Describe the morphology of the red blood cells.
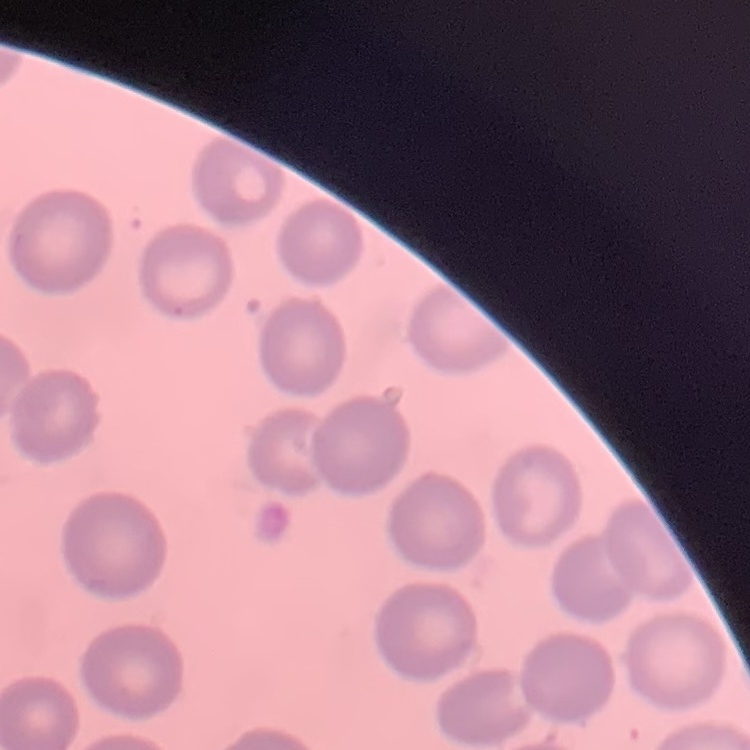
No rouleaux formation.

Thin blood film. One tile cut from a larger photomicrograph. Field's or Giemsa stain.